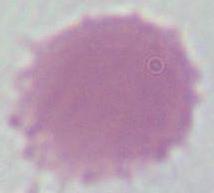
magnification = 1000x
identification = erythrocyte
modality = micrograph